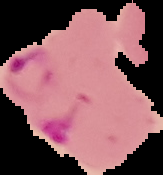
Segmented cell region on a black background. From a thin blood smear. Result: malaria parasites detected. Image is 163×175 pixels.